Describe the morphology of the erythrocytes.
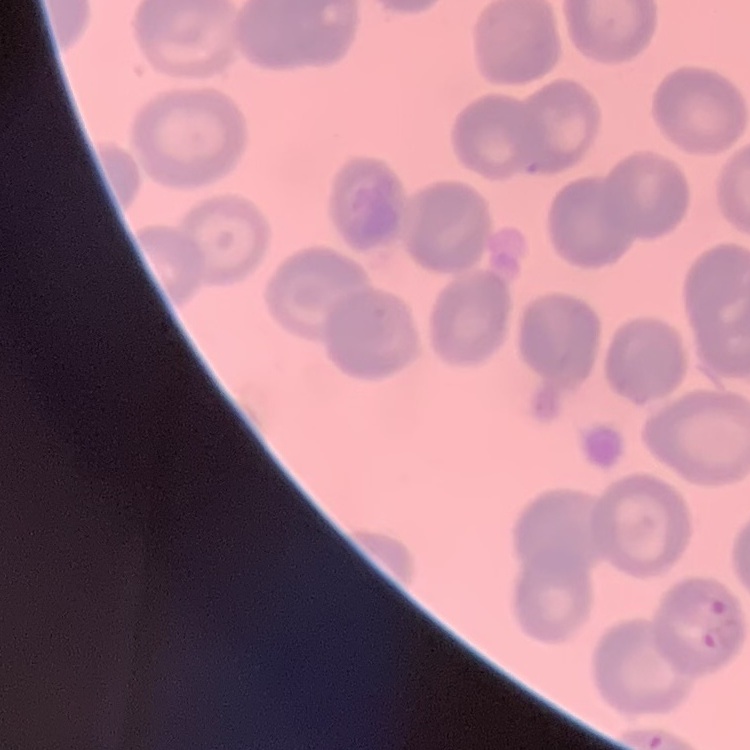
No rouleaux formation.

Summary:
  - Preparation: thin blood film
  - Image type: one tile cut from a larger photomicrograph
  - Stain: Field's or Giemsa